Name the parasite shown.
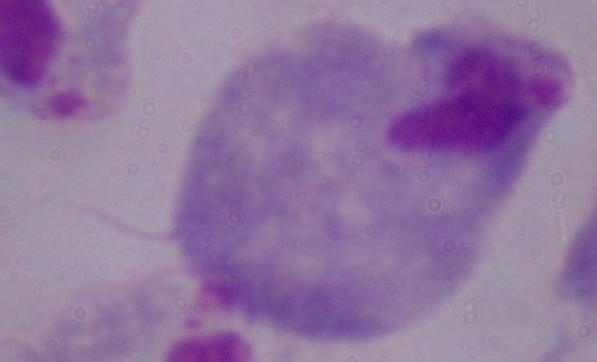

A trichomonad.

Summary:
  - Magnification: 1000x
  - Modality: micrograph